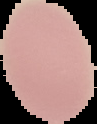
image size = 97×124 pixels
result = no Plasmodium parasites seen
image type = cell region segmented out of the field of view; surrounding area masked to black
preparation = thin blood film